Report the malaria status of this cell.
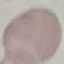

It is uninfected.

Summary:
  - Preparation: thin blood smear
  - Image type: automatically extracted cell patch, resized to 64 × 64 pixels
  - Capture: smartphone through the microscope eyepiece
  - Stain: Giemsa